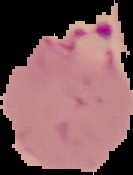

From a thin blood film. The area outside the segmented cell region is set to black. Result: malaria parasites detected. Image is 133×175 pixels.